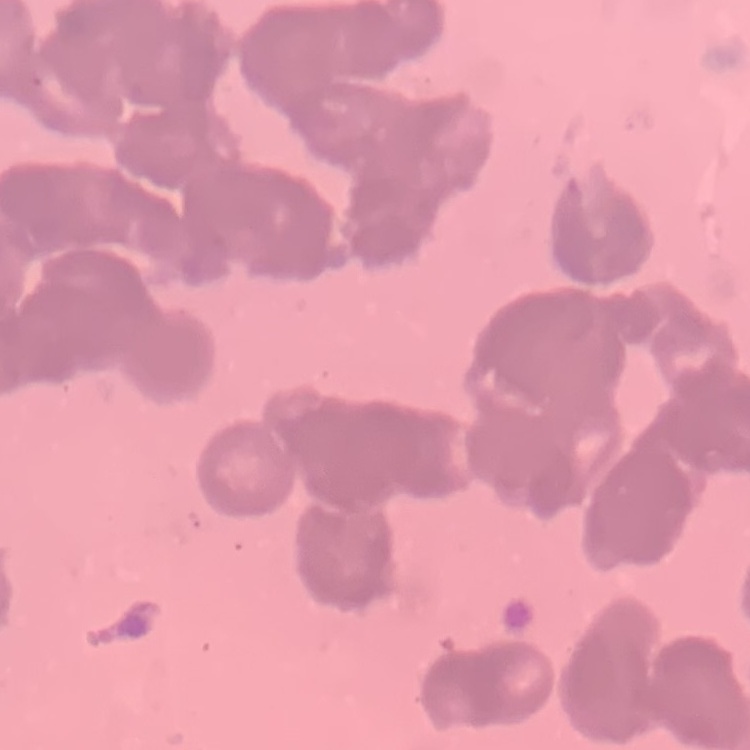

The red blood cells show rouleaux formation. Square crop of a larger photomicrograph. Thin peripheral smear. Field's or Giemsa stain.